Give the preparation type.
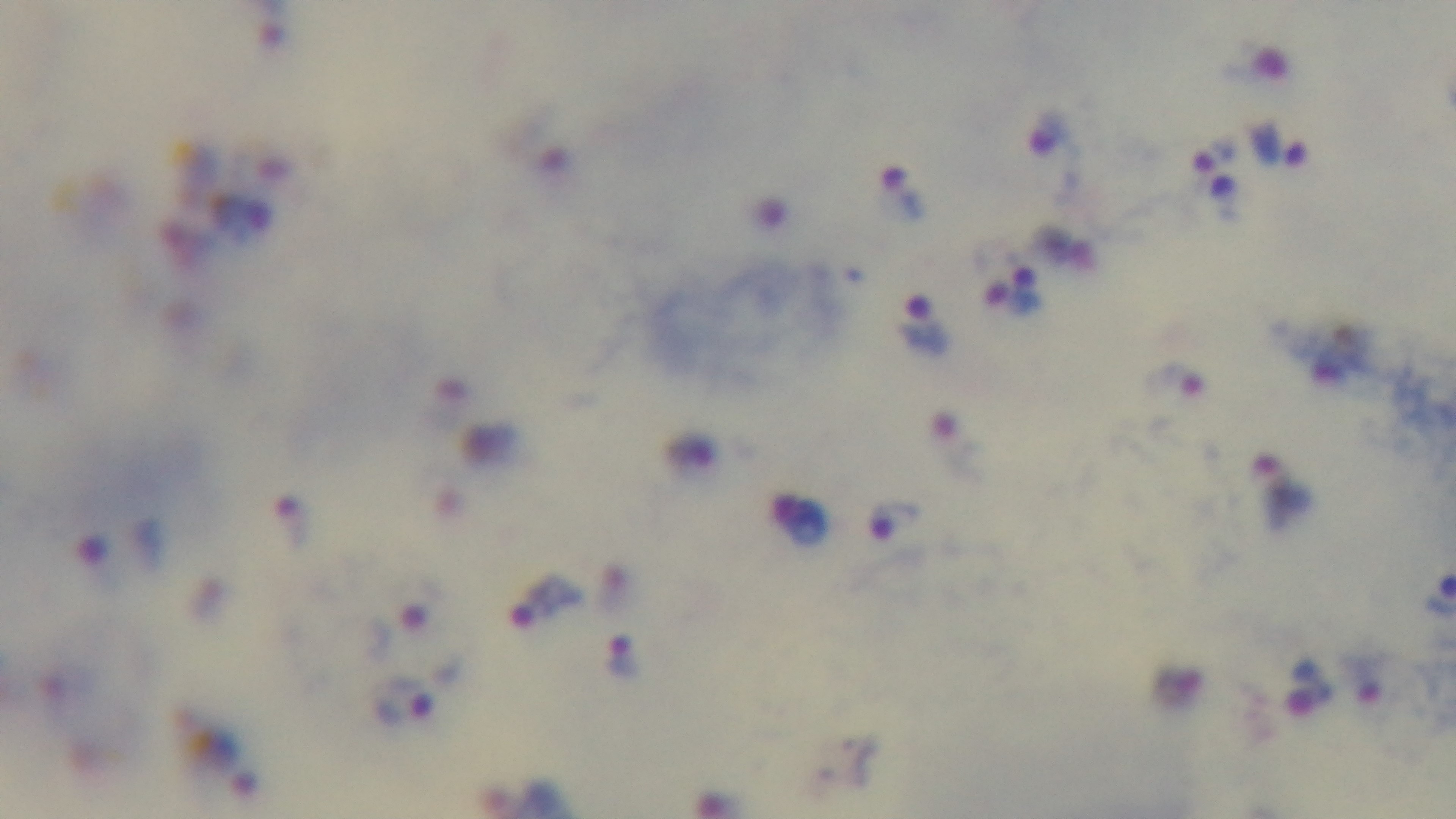
It is a thick blood film.

{
  "stain": "Giemsa",
  "malaria_status": "infected",
  "capture": "mounted 4K digital camera",
  "objective": "100x oil immersion",
  "field_of_view": "single",
  "modality": "light microscopy"
}